Report the malaria status of this cell.
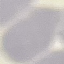
Uninfected.

preparation = thin blood film
image type = cell patch, automatically extracted from a larger field of view and resized to 64 × 64 pixels
capture = smartphone camera at the microscope eyepiece
stain = Giemsa